Comment on the morphology of the erythrocytes.
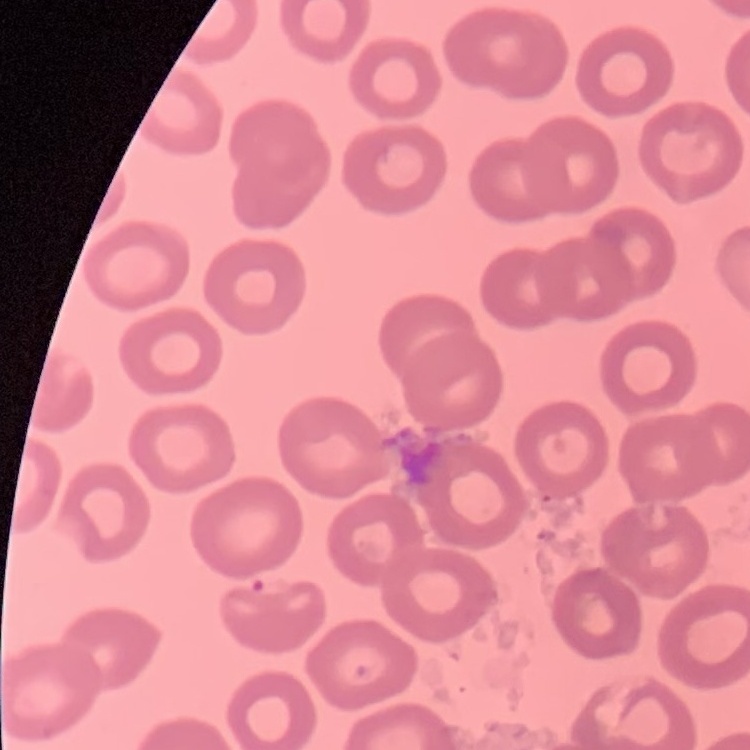

They show no rouleaux formation.

Thin blood film. Field's or Giemsa stain. One tile cut from a larger photomicrograph.